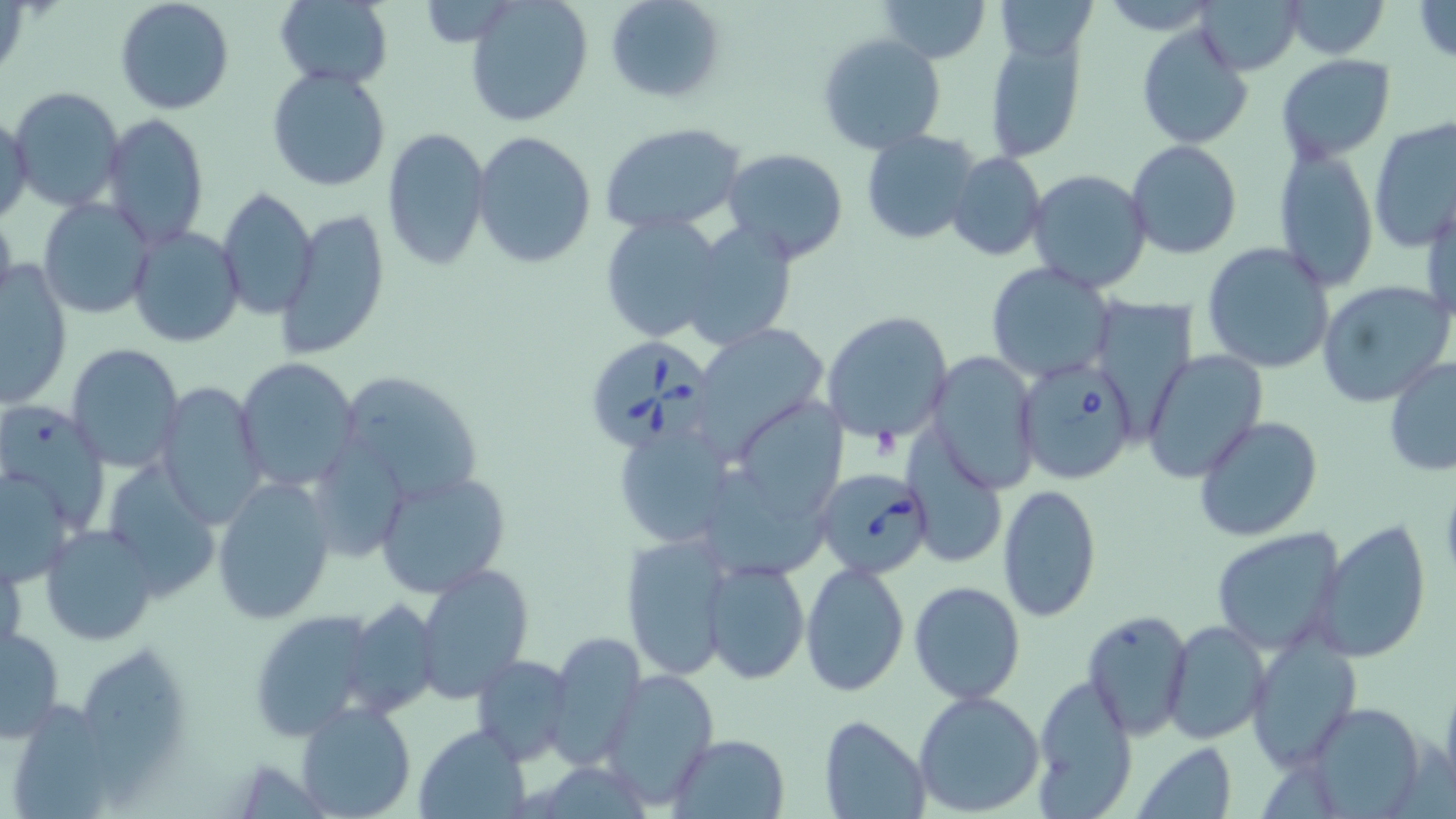

Summary:
  - Coordinate format: approximate bounding boxes as named x1/y1/x2/y2 corners in pixels
  - Uninfected red blood cell locations: (x1=115, y1=0, x2=234, y2=115), (x1=605, y1=0, x2=725, y2=105), (x1=877, y1=0, x2=990, y2=64), (x1=993, y1=0, x2=1100, y2=62), (x1=1281, y1=0, x2=1389, y2=58), (x1=1409, y1=0, x2=1456, y2=66), (x1=274, y1=1, x2=393, y2=88), (x1=1198, y1=1, x2=1301, y2=75), (x1=467, y1=2, x2=592, y2=125), (x1=1136, y1=24, x2=1251, y2=148), (x1=817, y1=32, x2=946, y2=155), (x1=983, y1=32, x2=1088, y2=165), (x1=1277, y1=54, x2=1395, y2=163), (x1=266, y1=67, x2=391, y2=192), (x1=7, y1=86, x2=125, y2=213), (x1=0, y1=112, x2=33, y2=224), (x1=102, y1=113, x2=209, y2=247), (x1=1368, y1=115, x2=1456, y2=252), (x1=601, y1=124, x2=748, y2=235), (x1=380, y1=128, x2=491, y2=271), (x1=861, y1=128, x2=980, y2=243), (x1=472, y1=130, x2=596, y2=269), (x1=1125, y1=140, x2=1245, y2=260), (x1=721, y1=147, x2=849, y2=265), (x1=1273, y1=147, x2=1381, y2=292), (x1=946, y1=151, x2=1046, y2=261), (x1=1024, y1=170, x2=1152, y2=294), (x1=217, y1=185, x2=317, y2=319), (x1=1423, y1=194, x2=1455, y2=326), (x1=36, y1=196, x2=156, y2=319), (x1=277, y1=207, x2=390, y2=360), (x1=0, y1=208, x2=18, y2=314), (x1=598, y1=214, x2=723, y2=343), (x1=683, y1=222, x2=802, y2=349), (x1=128, y1=226, x2=244, y2=347), (x1=1200, y1=242, x2=1335, y2=375), (x1=0, y1=261, x2=71, y2=408), (x1=986, y1=263, x2=1116, y2=383), (x1=1317, y1=280, x2=1455, y2=406), (x1=822, y1=310, x2=953, y2=446), (x1=704, y1=324, x2=830, y2=454), (x1=66, y1=344, x2=184, y2=470), (x1=1141, y1=349, x2=1269, y2=483), (x1=927, y1=352, x2=1040, y2=490), (x1=1384, y1=357, x2=1456, y2=478), (x1=232, y1=359, x2=360, y2=489), (x1=336, y1=371, x2=483, y2=506), (x1=152, y1=381, x2=267, y2=524), (x1=743, y1=400, x2=850, y2=517), (x1=1193, y1=415, x2=1323, y2=542), (x1=906, y1=433, x2=1008, y2=568), (x1=615, y1=435, x2=732, y2=541), (x1=103, y1=461, x2=223, y2=597), (x1=1, y1=468, x2=78, y2=587), (x1=376, y1=470, x2=512, y2=598), (x1=212, y1=476, x2=337, y2=625), (x1=995, y1=482, x2=1100, y2=621), (x1=1315, y1=519, x2=1432, y2=664), (x1=39, y1=524, x2=159, y2=645), (x1=1210, y1=527, x2=1346, y2=655), (x1=617, y1=537, x2=736, y2=679), (x1=1, y1=548, x2=24, y2=661), (x1=702, y1=559, x2=809, y2=684), (x1=802, y1=561, x2=909, y2=696), (x1=415, y1=564, x2=532, y2=704), (x1=908, y1=581, x2=1026, y2=705), (x1=339, y1=597, x2=440, y2=718), (x1=246, y1=610, x2=383, y2=742), (x1=1082, y1=610, x2=1193, y2=739), (x1=1162, y1=619, x2=1270, y2=746), (x1=1, y1=624, x2=67, y2=742), (x1=546, y1=632, x2=645, y2=767), (x1=1246, y1=635, x2=1362, y2=769), (x1=471, y1=654, x2=575, y2=765), (x1=602, y1=667, x2=718, y2=803), (x1=1439, y1=673, x2=1456, y2=799), (x1=1029, y1=675, x2=1138, y2=812), (x1=912, y1=689, x2=1046, y2=817), (x1=296, y1=701, x2=417, y2=819), (x1=1298, y1=701, x2=1430, y2=815), (x1=819, y1=716, x2=931, y2=818), (x1=415, y1=723, x2=531, y2=818), (x1=667, y1=734, x2=790, y2=819), (x1=1133, y1=742, x2=1239, y2=817)
  - Platelet locations: (x1=871, y1=424, x2=902, y2=460)
  - Babesia divergens-infected red blood cell locations: (x1=585, y1=336, x2=709, y2=451), (x1=1019, y1=362, x2=1140, y2=483), (x1=826, y1=466, x2=932, y2=573)
  - Slide-level diagnosis: Babesia divergens
  - Modality: light microscopy
  - Magnification: 1000x
  - Field of view: single
  - Stain: May-Grünwald-Giemsa
  - Preparation: thin blood film
  - Image size: 1456×819 pixels